Locate every parasitized red blood cell.
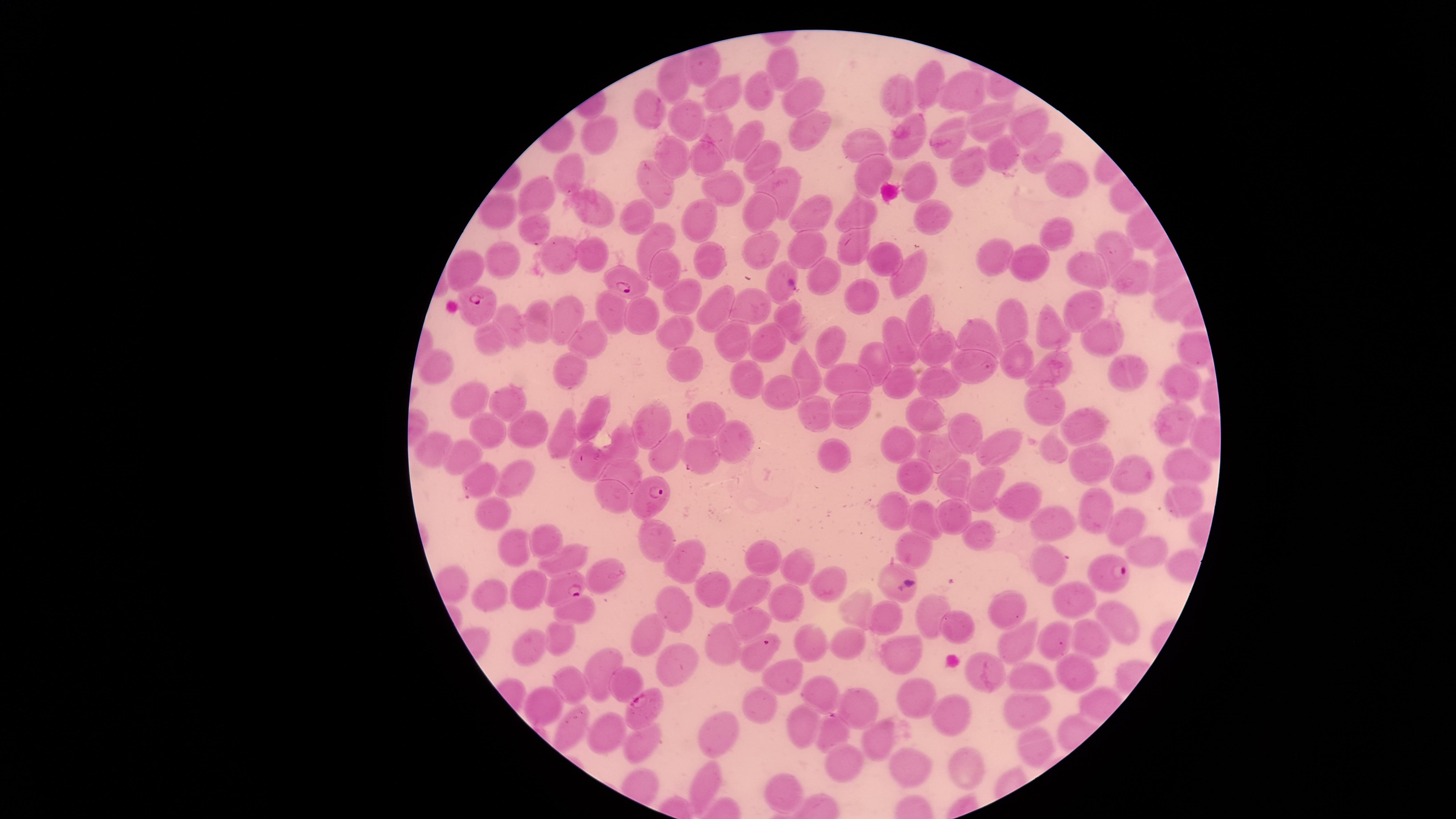
Approximate marker points as (x, y) in pixels.
Parasitized red blood cells: (619, 277), (478, 308), (650, 503), (1102, 574), (563, 589), (760, 646), (641, 712).

species = Plasmodium falciparum
uninfected red blood cells = approximate marker points as (x, y) in pixels: (790, 69), (669, 77), (929, 86), (962, 88), (761, 92), (797, 94), (901, 95), (723, 101), (648, 111), (687, 120), (987, 123), (1027, 126), (956, 132), (719, 133), (807, 135), (598, 136), (862, 140), (746, 143), (904, 144), (1047, 150), (1005, 154), (758, 158), (670, 159), (710, 162), (566, 168), (972, 171), (875, 173), (1060, 177), (779, 182), (924, 182), (653, 184), (718, 186), (533, 196), (593, 209), (495, 212), (759, 212), (858, 214), (813, 215), (934, 215), (636, 222), (689, 223), (534, 228), (1051, 234), (655, 240), (766, 247), (1110, 247), (855, 248), (804, 249), (588, 257), (555, 258), (991, 258), (504, 260), (1032, 260), (884, 261), (707, 262), (659, 267), (1082, 267), (904, 269), (825, 271), (473, 272), (779, 274), (1132, 278), (865, 296), (1079, 301), (682, 302), (723, 309), (755, 309), (608, 310), (920, 313), (642, 315), (794, 318), (539, 319), (569, 321), (513, 324), (674, 331), (1105, 333), (1045, 334), (1017, 335), (980, 337), (594, 339), (896, 339), (486, 340), (737, 341), (830, 343), (773, 345), (928, 346), (682, 361), (876, 363), (1012, 363), (974, 364), (437, 366), (571, 367), (1049, 367), (801, 370), (1122, 370), (846, 377), (942, 378), (742, 379), (904, 381), (1182, 384), (462, 389), (786, 392), (515, 406), (1036, 407), (845, 408), (813, 411), (595, 412), (919, 414), (695, 418), (532, 422), (651, 422), (1170, 428), (492, 429), (564, 429), (1088, 433), (970, 435), (733, 442), (623, 445), (429, 446), (668, 447), (1005, 447), (898, 448), (1050, 448), (701, 451), (943, 453), (464, 456), (586, 460), (835, 461), (1194, 461), (1093, 466), (513, 471), (622, 474), (908, 474), (1143, 475), (950, 481), (487, 483), (611, 489), (987, 490), (1179, 497), (1017, 503), (890, 505), (1093, 507), (498, 511), (955, 518), (922, 520), (1051, 523), (1127, 524), (973, 534), (908, 537), (657, 542), (545, 543), (1142, 545), (518, 547), (573, 557), (761, 557), (694, 562), (1051, 563), (800, 568), (889, 574), (608, 575), (524, 585), (749, 585), (714, 587), (828, 587), (1059, 591), (488, 595), (788, 601), (673, 606), (857, 607), (928, 609), (1009, 609), (573, 612), (1110, 617), (887, 618), (751, 619), (958, 625), (1014, 630), (642, 635), (1056, 640), (559, 641), (807, 642), (529, 644), (1096, 644), (850, 646), (725, 651), (900, 651), (676, 665), (602, 666), (1076, 667), (1026, 673), (987, 675), (780, 677), (630, 680), (571, 683), (822, 691), (914, 693), (545, 700), (859, 704), (1037, 705), (764, 707), (953, 713), (800, 725), (719, 728), (572, 730), (823, 732), (606, 735), (879, 736), (639, 745), (1032, 749), (839, 765), (910, 767), (970, 767), (705, 777), (788, 789)
visible region = circular
image size = 1456×819 pixels
field of view = single
capture = smartphone photograph through the microscope eyepiece
stain = Giemsa
preparation = thin smear of blood